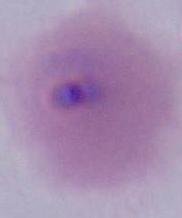

identification = Plasmodium
modality = micrograph
magnification = 400x or 1000x